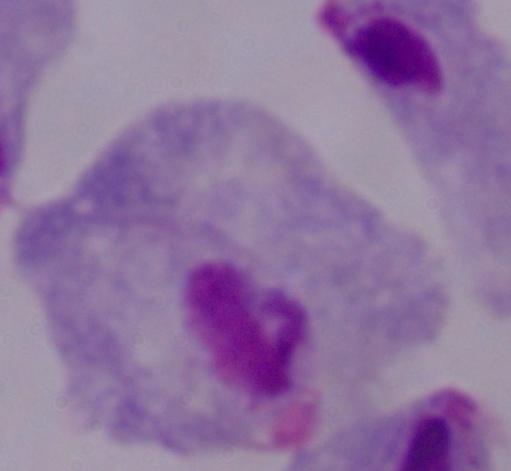

{
  "modality": "photomicrograph",
  "magnification": "1000x",
  "identification": "trichomonad"
}